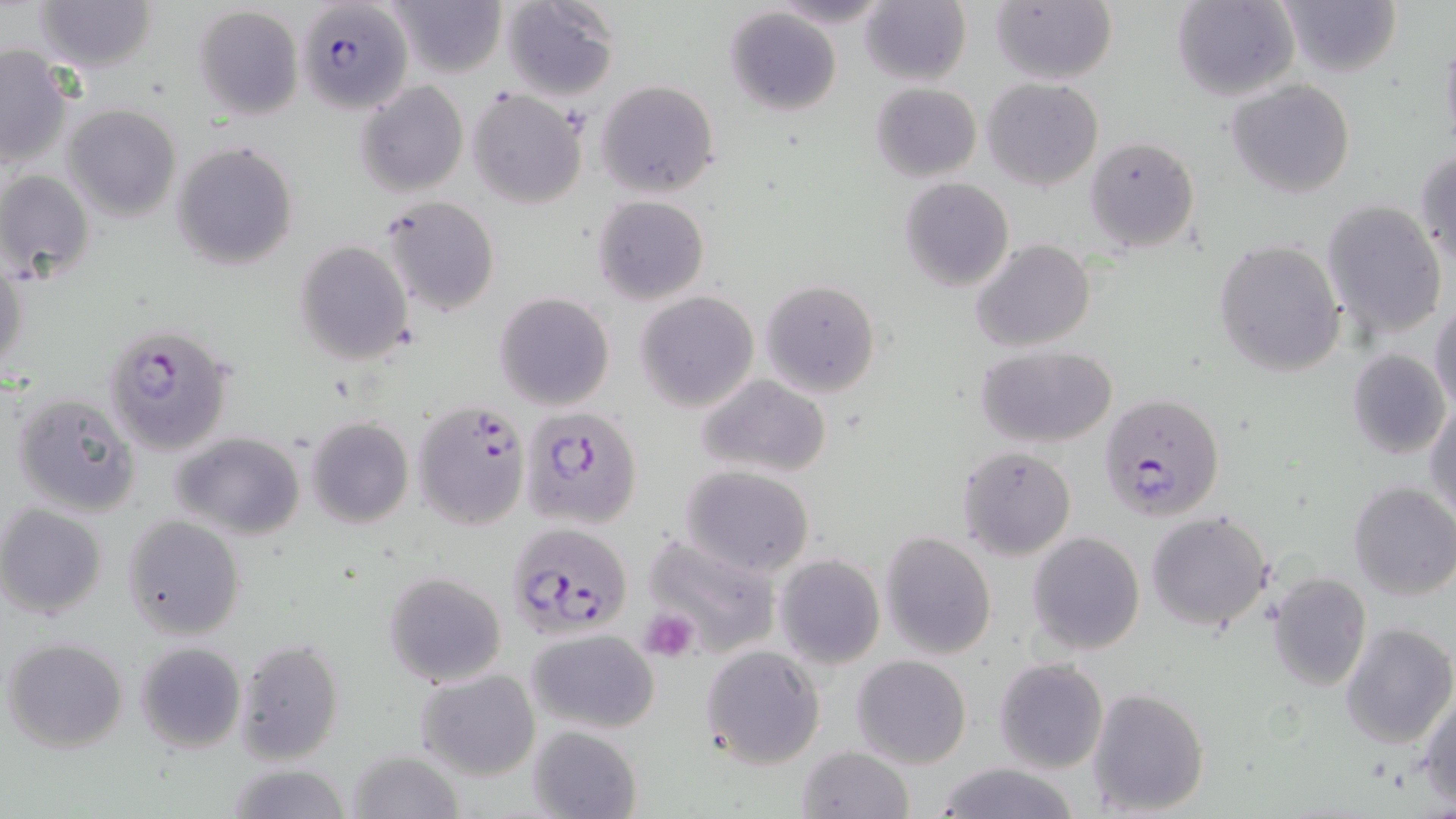

Approximate bounding boxes as (x1, y1, x2, y2) in pixels. Uninfected red blood cell locations: (32, 0, 157, 71), (390, 0, 504, 78), (499, 0, 620, 99), (1172, 0, 1299, 102), (1276, 0, 1401, 78), (861, 1, 971, 85), (991, 1, 1117, 85), (193, 7, 303, 123), (725, 7, 841, 116), (1439, 30, 1456, 162), (0, 45, 73, 168), (981, 78, 1104, 190), (596, 79, 720, 199), (1226, 79, 1355, 198), (355, 81, 468, 199), (869, 81, 981, 183), (467, 88, 589, 209), (63, 104, 181, 223), (1086, 136, 1199, 253), (171, 141, 298, 270), (1414, 147, 1456, 270), (0, 170, 94, 283), (899, 177, 1014, 292), (592, 195, 709, 305), (380, 196, 500, 317), (1320, 200, 1448, 339), (294, 239, 415, 367), (971, 239, 1096, 352), (1215, 240, 1345, 379), (0, 264, 28, 382), (760, 278, 881, 397), (634, 291, 760, 411), (494, 292, 615, 411), (1430, 301, 1456, 419), (974, 345, 1117, 447), (1346, 348, 1452, 461), (695, 374, 833, 480), (9, 391, 142, 518), (1426, 398, 1456, 528), (306, 417, 414, 529), (172, 431, 305, 539), (956, 444, 1077, 559), (681, 465, 815, 578), (1347, 480, 1456, 600), (0, 505, 107, 619), (1146, 510, 1273, 631), (122, 515, 245, 640), (642, 530, 780, 658), (1027, 531, 1145, 656), (880, 532, 997, 659), (774, 555, 885, 670), (382, 570, 509, 688), (1269, 573, 1371, 692), (1338, 622, 1454, 750), (526, 627, 660, 732), (3, 636, 129, 754), (234, 639, 344, 765), (136, 642, 246, 753), (700, 644, 826, 769), (851, 655, 972, 769), (994, 658, 1108, 773), (416, 669, 540, 780), (1087, 686, 1212, 816), (1418, 689, 1456, 808), (528, 726, 643, 819), (797, 745, 914, 819), (348, 748, 467, 819), (930, 761, 1087, 819), (224, 763, 352, 819). Platelet locations: (638, 608, 700, 663). Plasmodium falciparum-infected red blood cell locations: (295, 1, 412, 113), (103, 321, 233, 457), (1098, 391, 1225, 521), (412, 401, 531, 532), (522, 407, 642, 530), (505, 521, 632, 641). Slide-level diagnosis: Plasmodium falciparum. Single field of view. 1000x magnification. Thin blood smear. Image is 1456×819 pixels. Optical microscopy. May-Grünwald-Giemsa-stained preparation.